State which parasite is depicted.
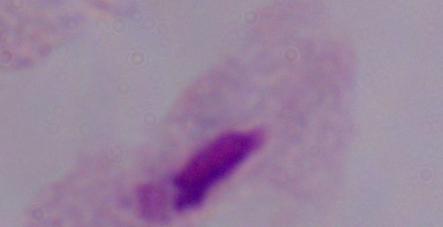
A trichomonad.

Photomicrograph. Captured at 1000x magnification.